Report the malaria status of this cell.
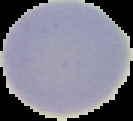
Uninfected.

image type = segmented cell region with the area outside set to black
image size = 133×121 pixels
preparation = thin blood smear